Assess the morphology of the erythrocytes.
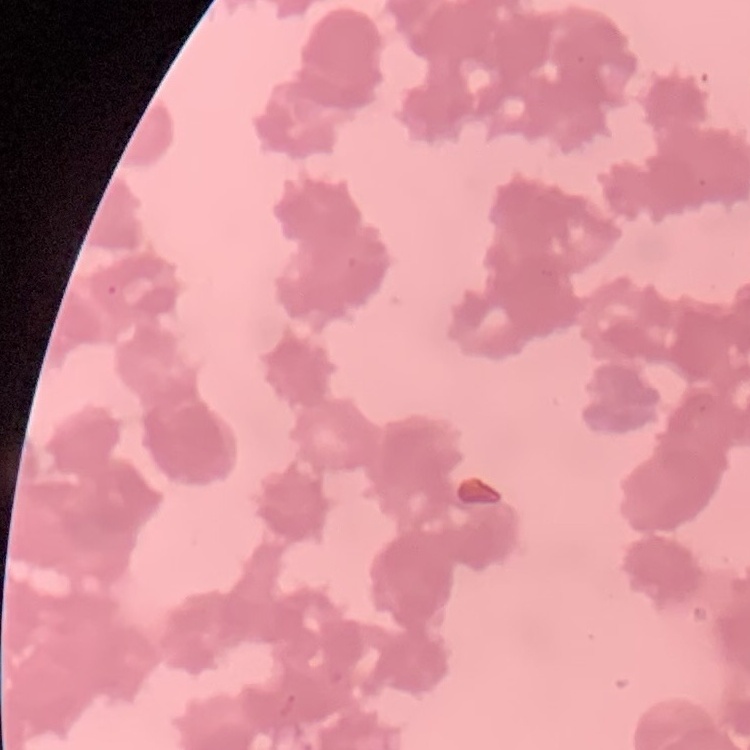

Rouleaux formation.

One tile cut from a larger photomicrograph. Thin blood film. Stained with either Field's or Giemsa.